Give the extent of all Plasmodium falciparum-infected red blood cells.
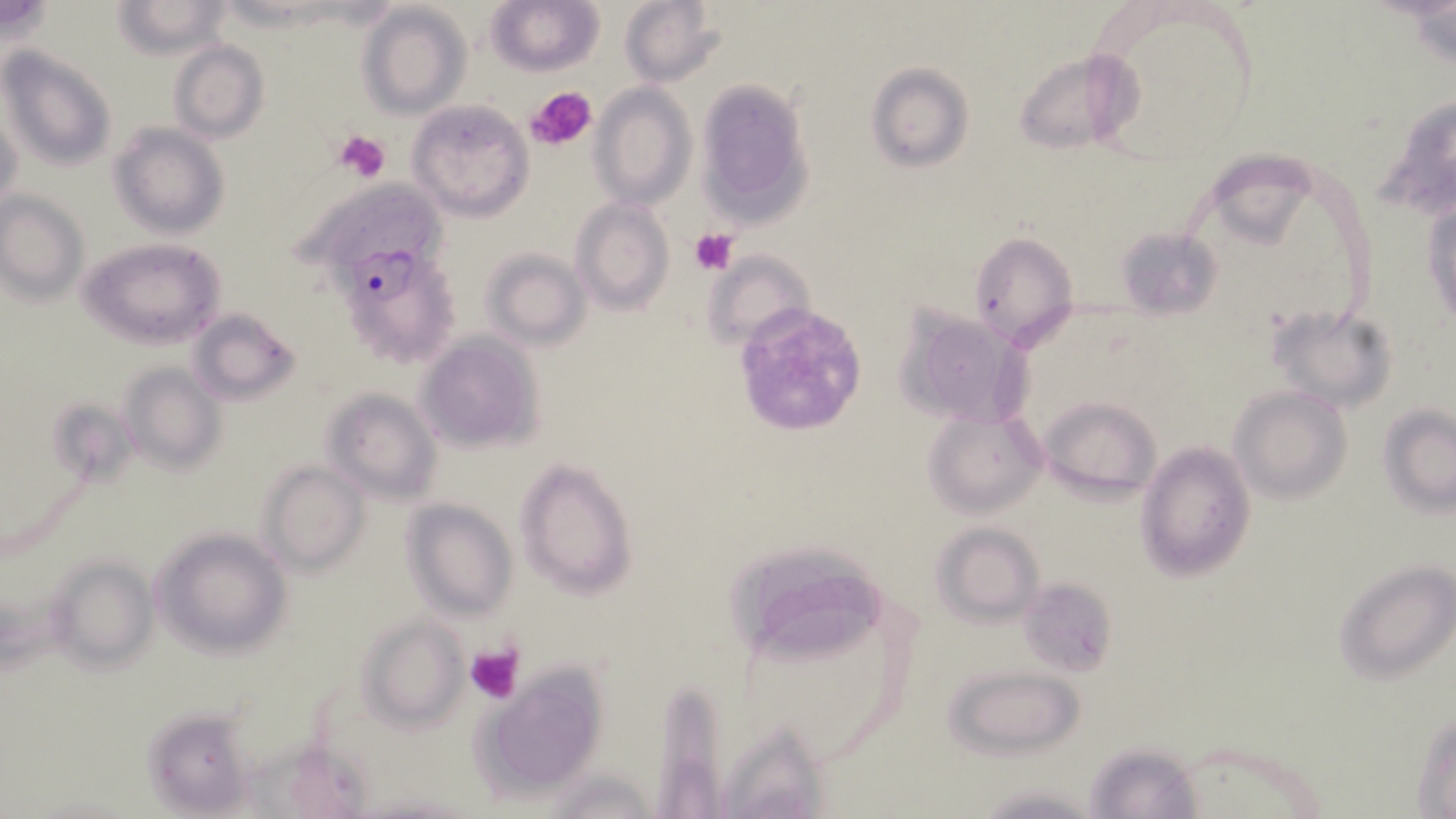

Approximate bounding boxes as named x1/y1/x2/y2 corners in pixels.
Plasmodium falciparum-infected red blood cells: (x1=333, y1=244, x2=457, y2=369).

slide_level_diagnosis: Plasmodium falciparum
stain: May-Grünwald-Giemsa
image_size: 1456×819 pixels
platelet_locations: 'approximate bounding boxes as named x1/y1/x2/y2 corners in pixels: (x1=527, y1=87, x2=598, y2=150), (x1=334, y1=130, x2=390, y2=182), (x1=691, y1=228, x2=738, y2=275), (x1=466, y1=644, x2=524, y2=705)'
modality: optical microscopy
uninfected_red_blood_cell_locations: 'approximate bounding boxes as named x1/y1/x2/y2 corners in pixels: (x1=487, y1=0, x2=603, y2=75), (x1=619, y1=0, x2=724, y2=86), (x1=115, y1=1, x2=232, y2=58), (x1=358, y1=4, x2=469, y2=119), (x1=169, y1=40, x2=268, y2=144), (x1=1, y1=46, x2=115, y2=173), (x1=1014, y1=48, x2=1145, y2=155), (x1=865, y1=63, x2=974, y2=171), (x1=695, y1=79, x2=814, y2=226), (x1=589, y1=83, x2=696, y2=209), (x1=408, y1=99, x2=533, y2=221), (x1=1, y1=108, x2=24, y2=216), (x1=110, y1=122, x2=229, y2=240), (x1=298, y1=176, x2=453, y2=280), (x1=1423, y1=187, x2=1455, y2=333), (x1=0, y1=190, x2=88, y2=303), (x1=570, y1=199, x2=675, y2=315), (x1=1114, y1=224, x2=1227, y2=319), (x1=970, y1=232, x2=1079, y2=349), (x1=82, y1=238, x2=225, y2=349), (x1=481, y1=249, x2=589, y2=348), (x1=702, y1=249, x2=815, y2=350), (x1=894, y1=304, x2=1031, y2=427), (x1=1268, y1=304, x2=1397, y2=414), (x1=731, y1=306, x2=865, y2=437), (x1=190, y1=309, x2=300, y2=405), (x1=417, y1=334, x2=542, y2=452), (x1=121, y1=363, x2=226, y2=475), (x1=321, y1=387, x2=442, y2=503), (x1=1230, y1=387, x2=1351, y2=503), (x1=1039, y1=395, x2=1162, y2=500), (x1=1379, y1=404, x2=1456, y2=513), (x1=922, y1=410, x2=1047, y2=517), (x1=1135, y1=440, x2=1257, y2=581), (x1=514, y1=459, x2=637, y2=597), (x1=259, y1=461, x2=368, y2=575), (x1=403, y1=500, x2=517, y2=621), (x1=933, y1=522, x2=1045, y2=624), (x1=154, y1=529, x2=292, y2=658), (x1=729, y1=544, x2=893, y2=657), (x1=46, y1=555, x2=157, y2=675), (x1=1334, y1=559, x2=1455, y2=684), (x1=1018, y1=579, x2=1117, y2=676), (x1=361, y1=618, x2=466, y2=730), (x1=942, y1=663, x2=1085, y2=759), (x1=480, y1=668, x2=606, y2=796), (x1=654, y1=680, x2=723, y2=819), (x1=147, y1=706, x2=253, y2=811), (x1=1412, y1=706, x2=1456, y2=818), (x1=716, y1=721, x2=839, y2=816), (x1=1084, y1=739, x2=1204, y2=818), (x1=233, y1=745, x2=374, y2=819), (x1=545, y1=766, x2=660, y2=819), (x1=968, y1=782, x2=1108, y2=816)'
preparation: thin blood smear
magnification: 1000x
field_of_view: one of a larger specimen